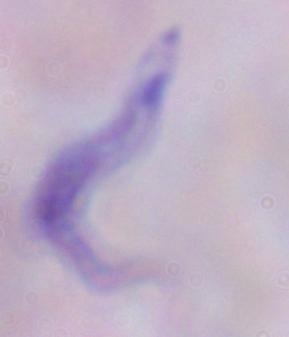
Photomicrograph. 1000x magnification. A trypanosome is seen.